Classify this cell by malaria status.
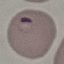

It is parasitized.

Summary:
  - Capture: smartphone through the microscope eyepiece
  - Stain: Giemsa
  - Image type: cell patch, automatically extracted from a larger field of view and resized to 64 × 64 pixels
  - Preparation: thin smear